Locate every blood parasite and identify its species.
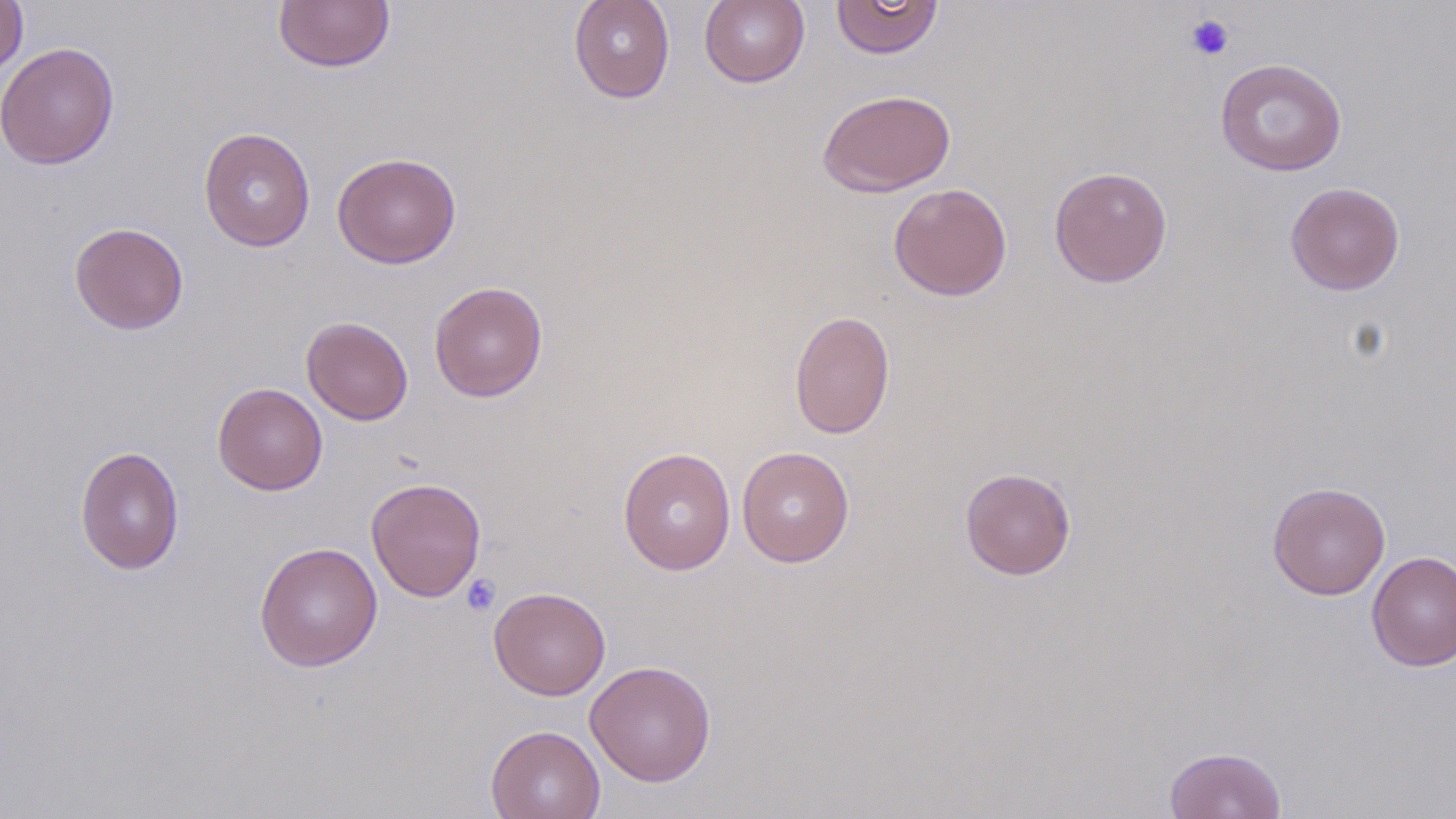

No blood parasites seen.

Approximate bounding boxes as (x1,y1)-(x2,y2) corner pairs in pixels. Platelet locations: (1185,13)-(1235,61), (461,574)-(501,616). Uninfected red blood cell locations: (0,0)-(28,79), (273,0)-(396,73), (569,0)-(675,103), (699,0)-(810,88), (830,0)-(944,59), (1,42)-(120,170), (1215,58)-(1347,176), (817,88)-(956,197), (199,126)-(316,253), (332,152)-(461,269), (1049,167)-(1173,287), (888,182)-(1012,301), (1285,182)-(1405,295), (69,221)-(189,335), (428,281)-(547,402), (789,309)-(895,439), (301,316)-(413,425), (212,382)-(328,495), (75,445)-(184,574), (736,446)-(854,567), (618,447)-(736,575), (959,467)-(1076,580), (366,477)-(487,602), (1267,481)-(1390,600), (254,541)-(383,672), (1366,550)-(1456,672), (489,586)-(611,700), (585,660)-(716,786), (485,724)-(606,819), (1164,746)-(1287,819). Slide-level diagnosis: negative for blood parasites. May-Grünwald-Giemsa stain. Thin blood smear. Single field of view. Captured at 1000x magnification. Image is 1456×819 pixels. Light microscopy.